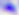
identification = Toxoplasma gondii
magnification = 400x
modality = photomicrograph